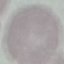
result = no malaria parasites detected
stain = Giemsa
image type = automatically extracted cell patch, resized to 64 × 64 pixels
preparation = thin blood film
capture = smartphone camera at the microscope eyepiece